Outline each Plasmodium falciparum-infected red blood cell.
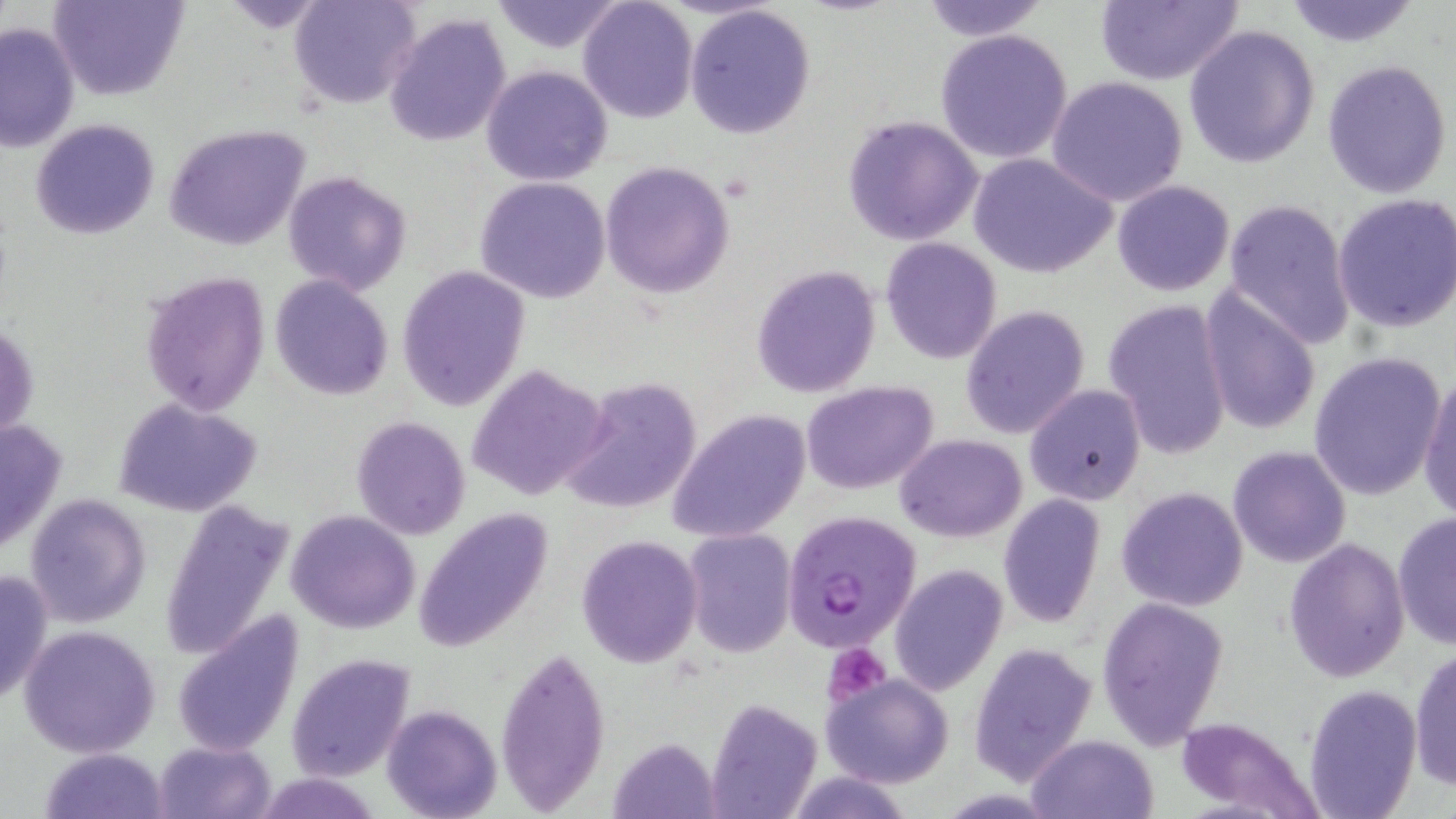
Approximate bounding boxes as (x1,y1)-(x2,y2) corner pairs in pixels.
Plasmodium falciparum-infected red blood cells: (780,509)-(921,652).

Platelet locations: (824,641)-(892,705). Uninfected red blood cell locations: (50,0)-(189,102), (489,0)-(627,53), (916,0)-(1053,42), (1094,0)-(1246,87), (1280,0)-(1423,49), (289,1)-(420,111), (579,1)-(698,123), (685,4)-(816,140), (383,12)-(512,148), (0,21)-(80,155), (1183,24)-(1319,168), (935,29)-(1073,164), (1322,58)-(1453,200), (482,65)-(613,186), (1047,76)-(1188,207), (842,113)-(984,247), (31,118)-(160,240), (164,124)-(311,252), (970,152)-(1118,279), (599,161)-(735,299), (282,170)-(411,296), (475,177)-(611,303), (1112,180)-(1235,296), (1332,192)-(1456,332), (1224,197)-(1355,348), (880,237)-(1002,365), (750,263)-(881,398), (396,267)-(530,411), (139,273)-(269,415), (269,274)-(393,401), (1199,287)-(1321,439), (1103,298)-(1232,460), (960,304)-(1091,439), (1,320)-(40,444), (1307,351)-(1446,500), (466,364)-(610,502), (1417,370)-(1456,524), (560,378)-(704,515), (800,382)-(939,495), (1024,385)-(1146,505), (112,396)-(262,517), (669,408)-(812,544), (1,415)-(64,561), (350,416)-(472,540), (895,433)-(1026,541), (1228,445)-(1350,568), (1117,485)-(1248,611), (25,494)-(150,628), (997,496)-(1105,628), (158,501)-(294,664), (412,508)-(554,655), (1391,509)-(1456,652), (285,510)-(421,634), (681,528)-(797,659), (577,533)-(704,668), (1283,538)-(1410,684), (889,564)-(1008,696), (0,568)-(51,708), (1095,597)-(1228,748), (173,609)-(304,756), (20,624)-(160,757), (495,643)-(610,813), (969,643)-(1099,785), (1410,645)-(1456,791), (286,654)-(414,781), (821,673)-(954,788), (1305,688)-(1421,819), (703,698)-(824,818), (382,704)-(503,819), (1172,715)-(1322,818), (1027,733)-(1159,819), (154,740)-(274,819), (39,748)-(167,818). Slide-level diagnosis: Plasmodium falciparum. Single field of view. May-Grünwald-Giemsa stain. 1000x magnification. Optical microscopy. Image is 1456×819 pixels. Thin blood smear.